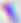
Summary:
  - Modality: photomicrograph
  - Magnification: 400x
  - Identification: Toxoplasma gondii